Assess this cell for malaria.
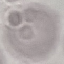

It is uninfected.

Giemsa-stained preparation. Acquired by smartphone through the microscope eyepiece. Cell patch, automatically extracted from a larger field of view and resized to 64 × 64 pixels. Thin smear of blood.